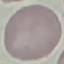
malaria status = uninfected
stain = Giemsa
capture = smartphone through the microscope eyepiece
preparation = thin blood film
image type = automatically extracted cell patch, resized to 64 × 64 pixels